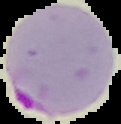

image type = segmented cell region on a black background
image size = 121×124 pixels
preparation = thin blood film
malaria status = parasitized